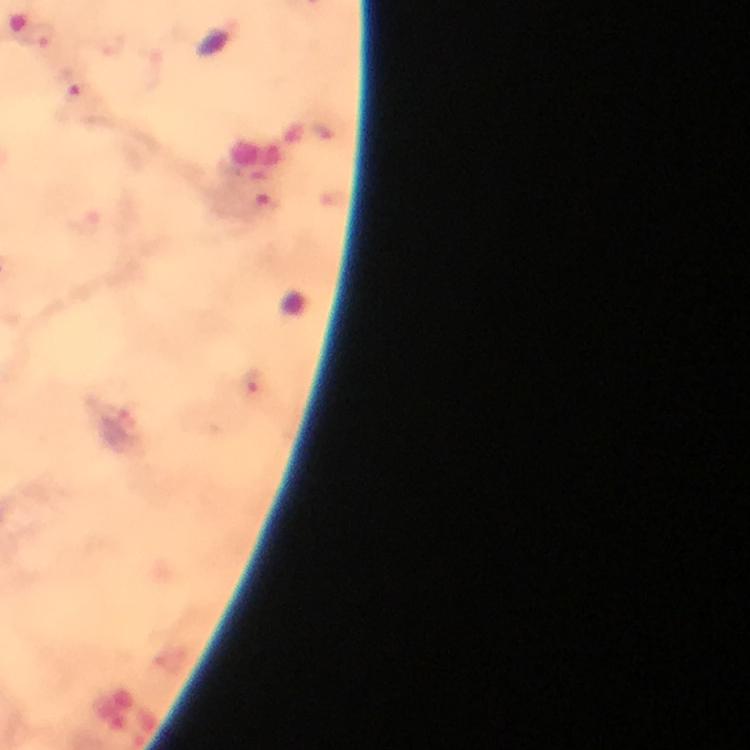
malaria parasite locations = approximate object centers, in pixels from the top-left corner: (x=42, y=36), (x=74, y=87), (x=266, y=205), (x=251, y=384)
immersion oil = used
cropped from = one field of view
stain = Giemsa
magnification = 100x
image size = 750×750 pixels
capture = smartphone photograph through a microscope
preparation = thick blood smear
context = from a diagnostic examination for malaria